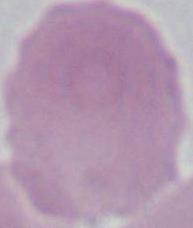

Photomicrograph. 1000x magnification. A red blood cell is seen.